Give the extent of all Plasmodium vivax-infected red blood cells.
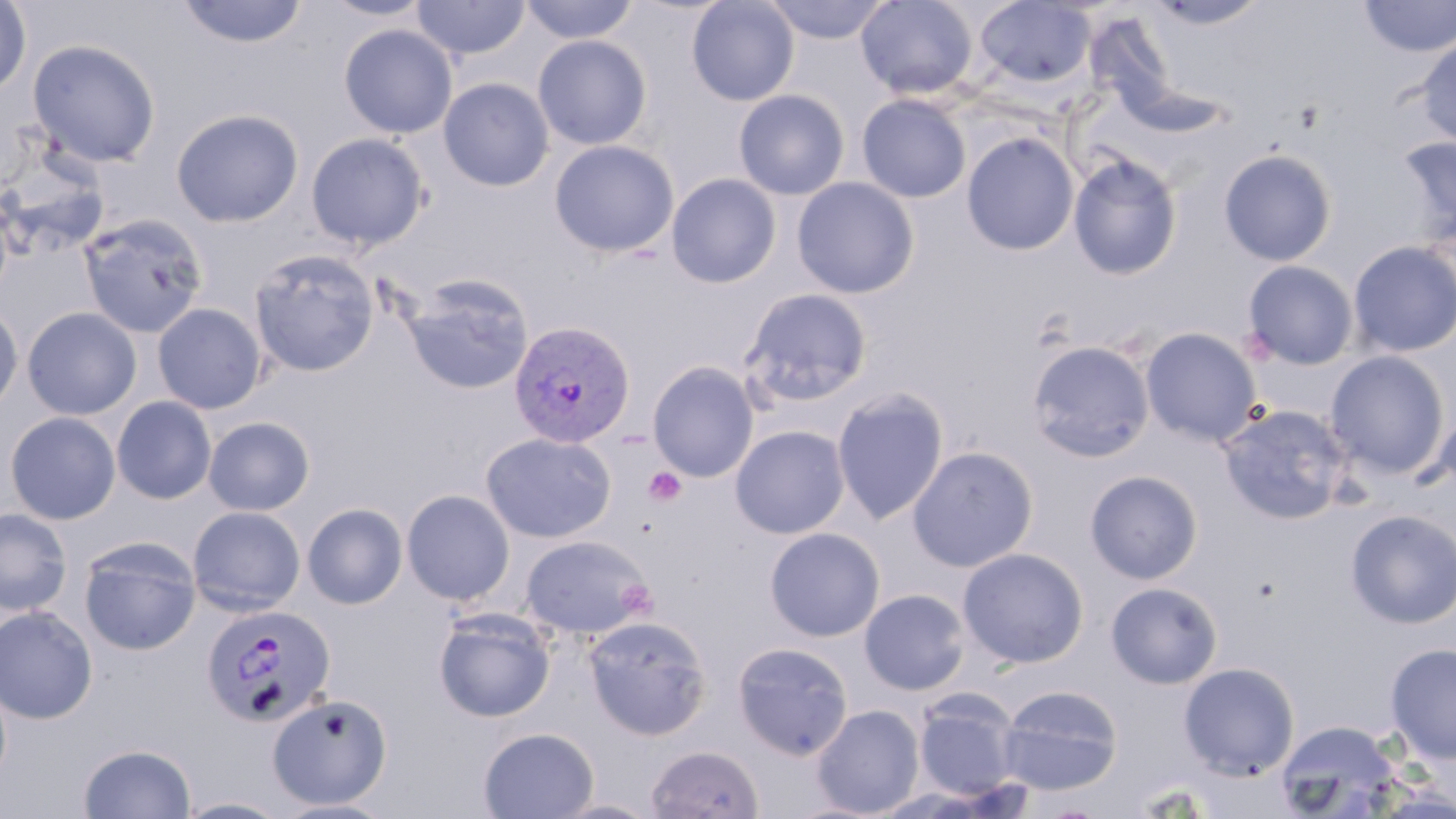
Approximate bounding boxes as (x1, y1, x2, y2) in pixels.
Plasmodium vivax-infected red blood cells: (508, 320, 636, 448), (201, 603, 335, 727).

{
  "slide_level_diagnosis": "Plasmodium vivax",
  "image_size": "1456×819 pixels",
  "uninfected_red_blood_cell_locations": "approximate bounding boxes as (x1, y1, x2, y2) in pixels: (320, 0, 434, 21), (412, 0, 530, 61), (519, 0, 640, 44), (686, 0, 800, 106), (764, 0, 891, 44), (855, 0, 979, 100), (975, 0, 1096, 89), (1146, 0, 1272, 30), (1357, 0, 1456, 59), (0, 1, 32, 96), (177, 1, 309, 49), (339, 23, 457, 139), (533, 35, 652, 150), (1414, 37, 1456, 147), (27, 39, 160, 167), (438, 77, 554, 191), (734, 88, 850, 200), (857, 94, 972, 203), (170, 108, 304, 228), (305, 132, 430, 250), (961, 132, 1080, 255), (1394, 135, 1456, 245), (549, 139, 680, 257), (1218, 149, 1338, 266), (1066, 152, 1183, 280), (1, 155, 111, 260), (666, 173, 782, 288), (791, 177, 920, 299), (0, 194, 13, 305), (79, 213, 209, 338), (1348, 240, 1456, 358), (248, 248, 380, 377), (1242, 260, 1359, 370), (404, 276, 534, 395), (740, 288, 873, 407), (0, 301, 24, 416), (152, 302, 267, 414), (22, 307, 142, 420), (1140, 327, 1262, 445), (1025, 340, 1156, 462), (1324, 350, 1451, 479), (647, 361, 760, 482), (831, 388, 950, 526), (112, 396, 216, 504), (1218, 403, 1354, 525), (1427, 403, 1456, 500), (4, 412, 121, 525), (203, 416, 315, 515), (730, 425, 850, 539), (480, 432, 616, 543), (907, 445, 1039, 572), (1084, 469, 1203, 584), (401, 489, 515, 605), (303, 503, 408, 609), (188, 506, 306, 615), (0, 507, 72, 616), (1345, 509, 1456, 628), (764, 527, 885, 642), (519, 534, 654, 639), (79, 538, 201, 655), (957, 547, 1089, 668), (1106, 581, 1223, 689), (859, 589, 970, 695), (1, 606, 98, 725), (434, 608, 555, 722), (582, 615, 713, 739), (731, 642, 853, 760), (1385, 642, 1456, 763), (1179, 662, 1299, 780), (997, 684, 1124, 795), (913, 690, 1022, 800), (267, 693, 393, 810), (812, 704, 924, 817), (1275, 720, 1401, 817), (479, 727, 599, 818), (645, 743, 765, 818), (79, 744, 196, 819), (175, 797, 292, 818), (549, 798, 662, 819), (273, 799, 398, 819)",
  "magnification": "1000x",
  "stain": "May-Grünwald-Giemsa",
  "modality": "light microscopy",
  "preparation": "thin blood film",
  "field_of_view": "one of a larger specimen"
}